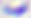 Photomicrograph. Toxoplasma gondii is shown. Captured at 400x magnification.